Identify the parasite.
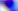
This is Toxoplasma gondii.

Summary:
  - Magnification: 400x
  - Modality: photomicrograph